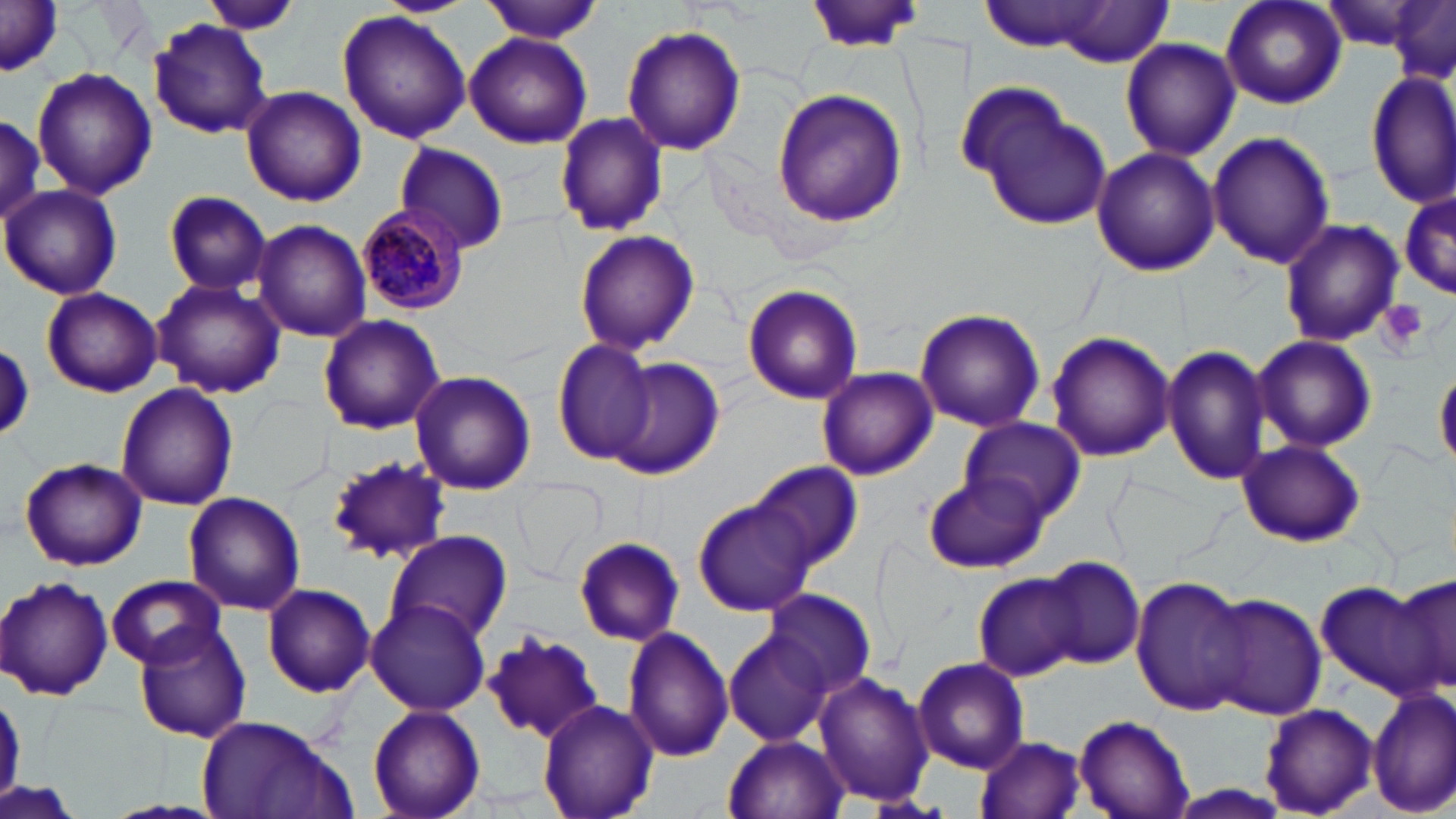
slide-level diagnosis = Plasmodium malariae
platelet locations = approximate bounding boxes as (x1, y1, x2, y2) in pixels: (1376, 299, 1430, 357)
modality = optical microscopy
magnification = 1000x
image size = 1456×819 pixels
field of view = one of a larger specimen
Plasmodium malariae-infected red blood cell locations = approximate bounding boxes as (x1, y1, x2, y2) in pixels: (355, 204, 470, 316)
stain = May-Grünwald-Giemsa
preparation = thin blood film
uninfected red blood cell locations = approximate bounding boxes as (x1, y1, x2, y2) in pixels: (202, 0, 302, 35), (374, 0, 474, 17), (480, 0, 604, 42), (806, 0, 925, 52), (1220, 0, 1347, 110), (978, 1, 1114, 53), (1387, 1, 1454, 83), (1, 2, 63, 75), (1053, 2, 1170, 69), (338, 11, 473, 143), (148, 19, 272, 139), (621, 25, 746, 157), (464, 31, 592, 147), (1120, 37, 1240, 162), (32, 66, 156, 200), (1369, 68, 1455, 209), (240, 84, 367, 207), (771, 89, 908, 227), (972, 93, 1113, 232), (0, 111, 45, 234), (553, 111, 666, 238), (1207, 131, 1333, 268), (393, 143, 511, 254), (1090, 146, 1218, 277), (1, 183, 123, 300), (1398, 184, 1454, 301), (163, 189, 273, 295), (1279, 217, 1404, 348), (252, 219, 371, 343), (573, 230, 700, 357), (153, 277, 286, 399), (742, 284, 864, 404), (42, 287, 162, 397), (914, 308, 1045, 432), (318, 315, 445, 435), (1045, 331, 1175, 464), (1252, 334, 1377, 454), (0, 340, 34, 442), (552, 340, 658, 467), (1162, 341, 1270, 486), (611, 357, 725, 480), (1435, 366, 1456, 469), (815, 367, 938, 480), (410, 371, 537, 496), (116, 383, 238, 510), (960, 415, 1085, 522), (1237, 439, 1366, 547), (325, 455, 450, 564), (20, 458, 147, 569), (751, 460, 862, 572), (922, 471, 1050, 573), (513, 477, 605, 581), (185, 493, 305, 614), (694, 498, 816, 618), (383, 529, 512, 647), (573, 536, 684, 646), (1039, 556, 1145, 670), (971, 572, 1083, 681), (1390, 572, 1456, 702), (107, 574, 225, 668), (1131, 575, 1249, 716), (2, 578, 115, 699), (1314, 580, 1438, 696), (261, 583, 374, 696), (764, 587, 877, 700), (1199, 593, 1326, 722), (365, 597, 491, 715), (131, 619, 252, 744), (623, 625, 735, 762), (483, 631, 608, 743), (725, 631, 834, 746), (913, 657, 1029, 774), (814, 670, 934, 806), (1368, 685, 1454, 817), (0, 688, 31, 796), (537, 700, 659, 819), (367, 704, 485, 819), (1259, 704, 1378, 816), (194, 712, 354, 819), (1074, 714, 1196, 819), (724, 734, 847, 819), (973, 736, 1086, 819), (1155, 784, 1298, 818)